Classify this cell by malaria status.
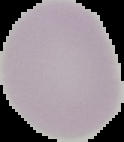
It is uninfected.

preparation: thin blood smear
image_size: 124×142 pixels
image_type: segmented cell region with the area outside set to black